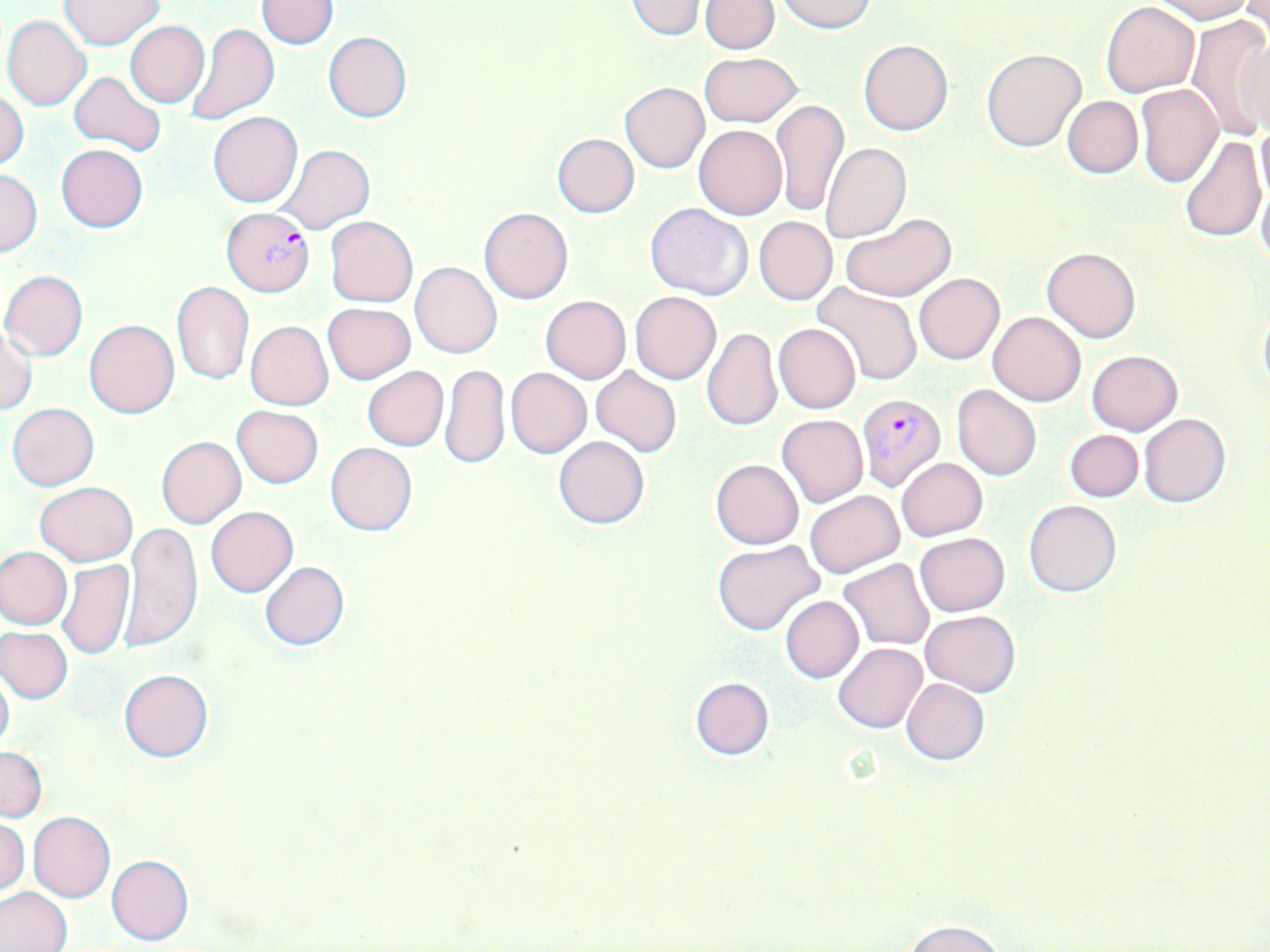

slide-level diagnosis = Plasmodium falciparum
stain = May-Grünwald-Giemsa
Plasmodium falciparum-infected red blood cell locations = approximate bounding boxes as [x1, y1, x2, y2] in pixels: [220, 207, 315, 297], [856, 391, 945, 492]
magnification = 1000x
preparation = thin blood film
uninfected red blood cell locations = approximate bounding boxes as [x1, y1, x2, y2] in pixels: [257, 0, 338, 50], [623, 0, 709, 40], [701, 0, 779, 53], [1150, 0, 1254, 23], [59, 1, 167, 49], [778, 1, 877, 33], [1101, 2, 1200, 97], [1238, 2, 1269, 41], [2, 15, 92, 110], [1186, 15, 1270, 140], [124, 20, 210, 108], [185, 22, 279, 127], [1229, 29, 1268, 139], [323, 31, 412, 122], [858, 39, 954, 136], [981, 47, 1087, 152], [699, 52, 802, 127], [1155, 58, 1257, 178], [70, 71, 166, 157], [619, 82, 710, 173], [1135, 84, 1223, 188], [0, 91, 28, 171], [1062, 95, 1143, 179], [772, 99, 847, 217], [207, 113, 302, 206], [1255, 118, 1270, 211], [693, 124, 787, 220], [551, 133, 640, 218], [1180, 135, 1266, 243], [820, 143, 911, 244], [56, 144, 148, 232], [276, 145, 375, 234], [1, 169, 42, 256], [1256, 172, 1270, 270], [646, 202, 752, 300], [479, 207, 573, 304], [839, 212, 957, 301], [754, 215, 837, 305], [324, 216, 417, 308], [1042, 246, 1140, 343], [410, 261, 501, 358], [0, 271, 89, 360], [914, 273, 1004, 365], [171, 282, 254, 386], [811, 282, 923, 390], [630, 292, 721, 384], [540, 295, 631, 383], [1258, 300, 1270, 400], [322, 303, 415, 386], [987, 311, 1085, 406], [84, 320, 179, 418], [245, 320, 333, 410], [1, 324, 37, 414], [773, 324, 861, 414], [702, 326, 781, 431], [1087, 349, 1182, 435], [439, 362, 510, 471], [590, 365, 682, 457], [361, 366, 448, 451], [506, 368, 590, 459], [951, 385, 1041, 481], [7, 403, 99, 490], [232, 405, 323, 488], [1139, 413, 1230, 508], [776, 414, 868, 508], [1064, 430, 1144, 502], [552, 435, 651, 529], [156, 436, 246, 528], [325, 442, 418, 536], [896, 457, 987, 542], [710, 459, 804, 549], [35, 482, 138, 565], [804, 490, 904, 580], [1023, 499, 1121, 598], [205, 505, 298, 597], [120, 522, 202, 654], [914, 532, 1011, 616], [711, 539, 825, 637], [0, 546, 71, 630], [56, 559, 135, 661], [838, 559, 934, 650], [259, 561, 349, 651], [780, 595, 863, 683], [920, 611, 1021, 696], [1, 625, 74, 705], [834, 643, 927, 734], [0, 665, 14, 759], [119, 668, 212, 761], [689, 677, 774, 759], [901, 678, 989, 765], [0, 746, 47, 822], [28, 811, 115, 903], [1, 816, 28, 896], [106, 854, 194, 946], [0, 886, 72, 952], [902, 918, 1007, 952]
modality = optical microscopy
image size = 1270×952 pixels
field of view = single